Describe the morphology of the erythrocytes.
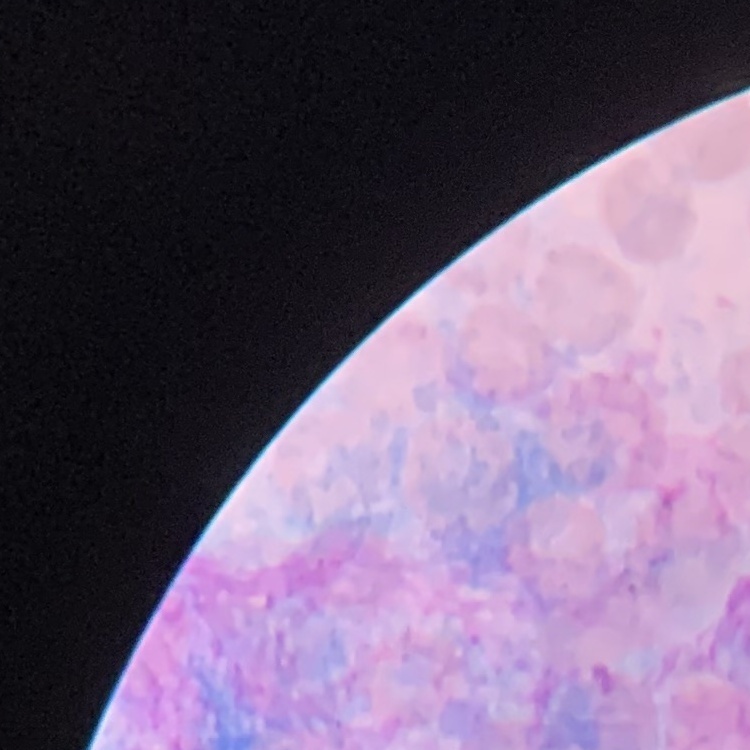
No rouleaux formation.

Field's or Giemsa stain. One tile cut from a larger photomicrograph. Thin peripheral smear.